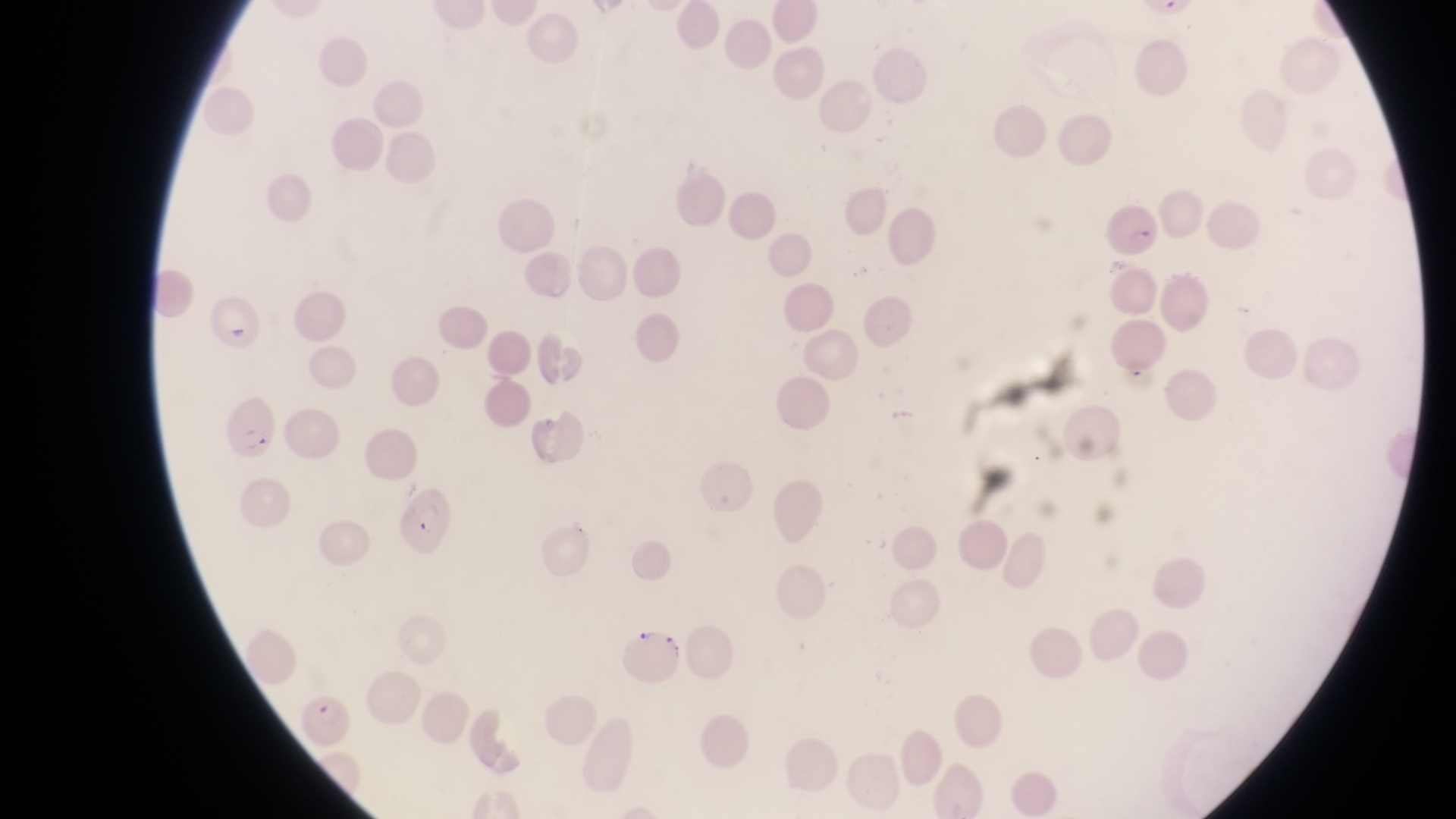 Approximate bounding boxes as [left, top, right, bottom] in pixels. Parasitised red blood cell locations: [1105, 201, 1161, 259], [228, 394, 280, 463], [391, 486, 452, 555], [620, 631, 686, 684], [293, 693, 357, 748]. Thin blood film. Magnification of 1000x. Photographed through the eyepiece of an Olympus CX-23 microscope with a smartphone camera. Single field of view. Image is 1456×819 pixels. Sample from Uganda.